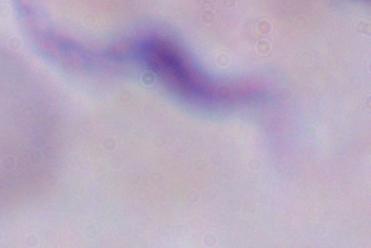

A trypanosome is shown. Captured at 1000x magnification. Photomicrograph.